Assess this cell for malaria.
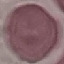
It is uninfected.

Summary:
  - Capture: smartphone camera at the microscope eyepiece
  - Stain: Giemsa
  - Image type: automatically extracted cell patch, resized to 64 × 64 pixels
  - Preparation: thin smear